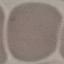

Result: negative for malaria parasites. Giemsa stain. Thin blood film. Automatically extracted cell patch, resized to 64 × 64 pixels. Photographed with a smartphone camera at the microscope eyepiece.